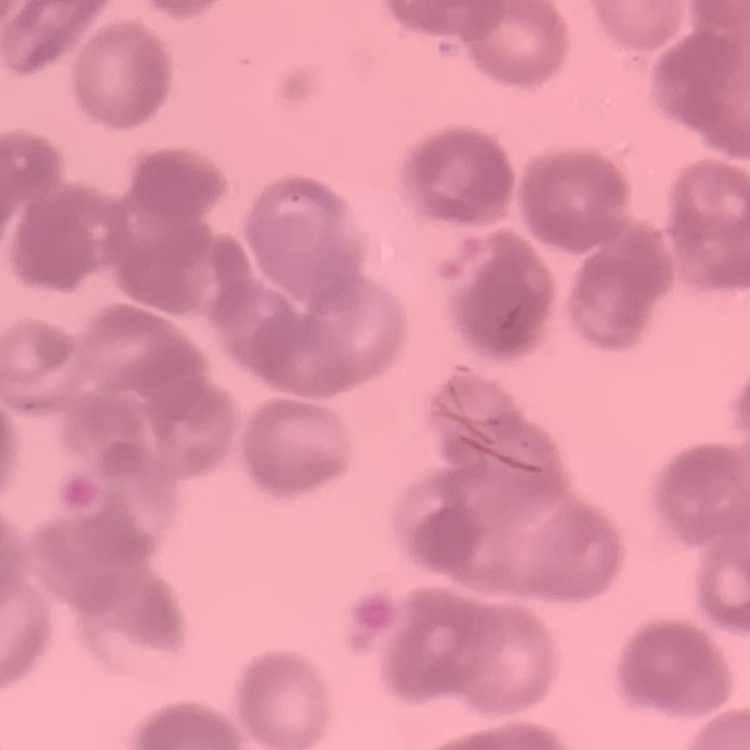

red blood cell morphology = rouleaux formation
stain = Field's or Giemsa
image type = one tile cut from a larger photomicrograph
preparation = thin blood film